Comment on the morphology of the red blood cells.
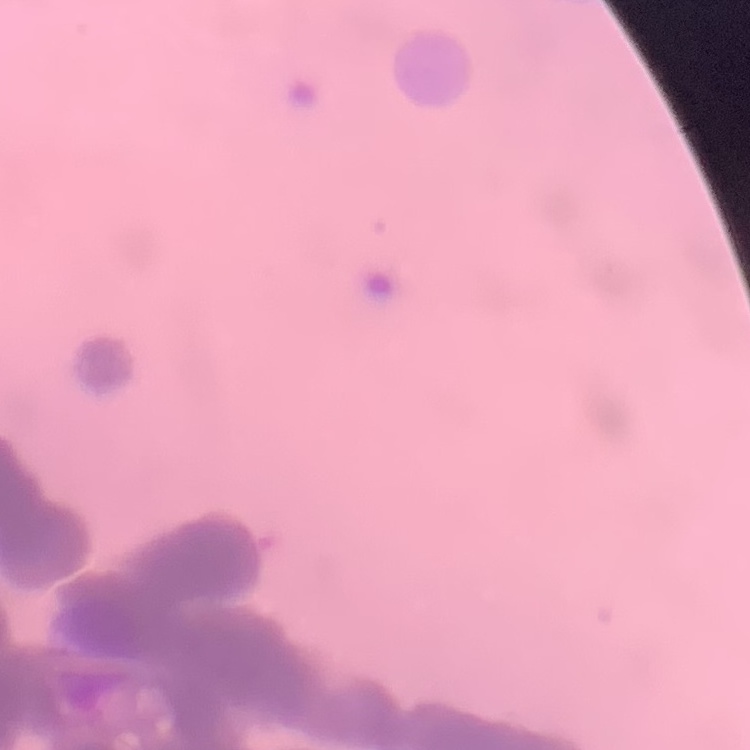
Rouleaux formation.

Thin peripheral smear. One tile cut from a larger photomicrograph. Field's or Giemsa stain.